Classify this cell by malaria status.
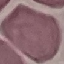

It is uninfected.

Photographed with a smartphone camera at the microscope eyepiece. Giemsa stain. Automatically extracted cell patch, resized to 64 × 64 pixels. Thin blood smear.